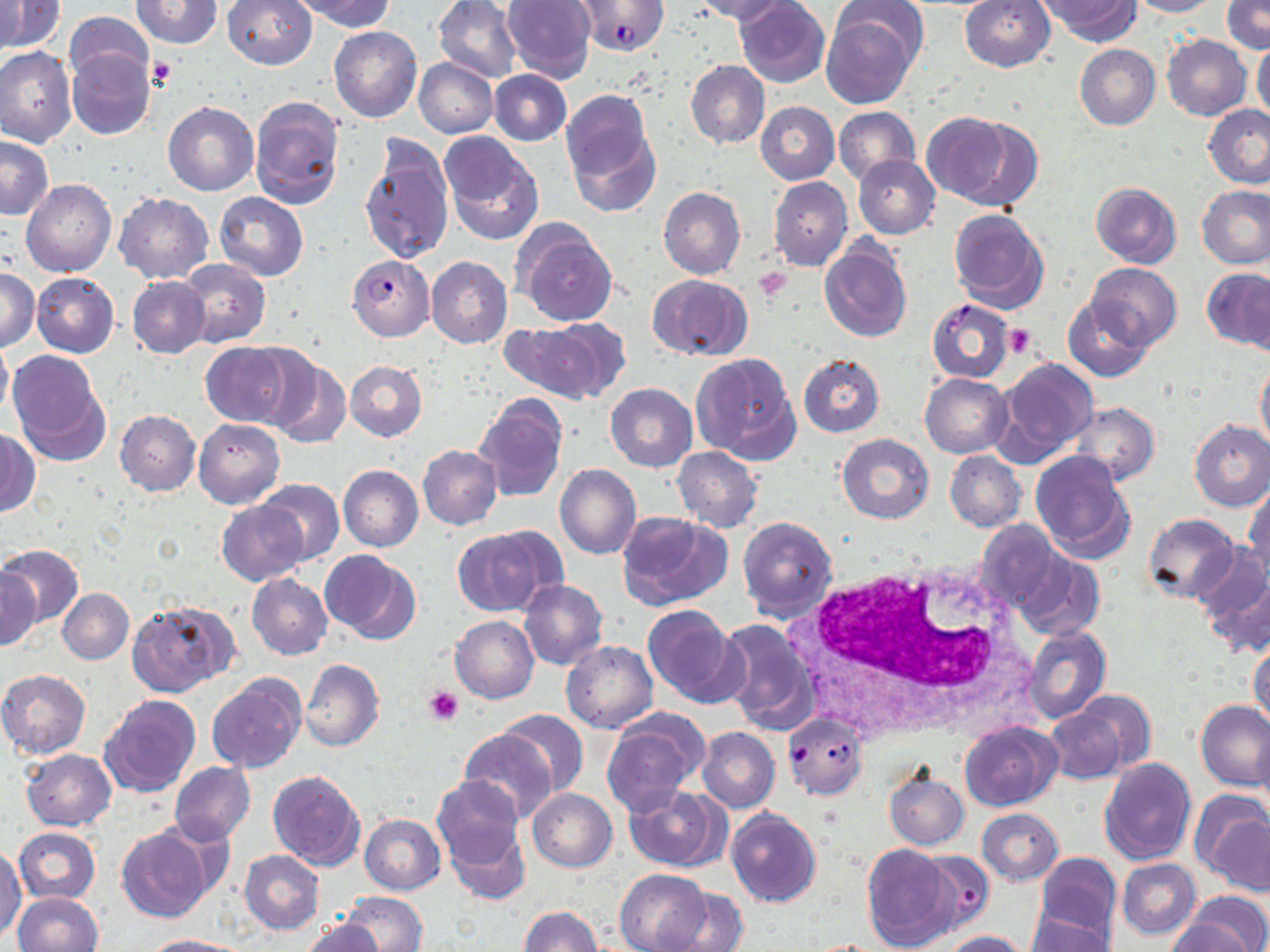
Approximate bounding boxes as named x1/y1/x2/y2 corners in pixels. White blood cell locations: (x1=792, y1=554, x2=1030, y2=734). Platelet locations: (x1=147, y1=57, x2=177, y2=90), (x1=753, y1=265, x2=794, y2=302), (x1=1003, y1=324, x2=1036, y2=359), (x1=422, y1=686, x2=464, y2=726). Uninfected red blood cell locations: (x1=132, y1=0, x2=222, y2=47), (x1=222, y1=0, x2=318, y2=70), (x1=433, y1=0, x2=522, y2=83), (x1=503, y1=0, x2=596, y2=81), (x1=734, y1=0, x2=829, y2=87), (x1=959, y1=0, x2=1055, y2=72), (x1=1129, y1=0, x2=1221, y2=18), (x1=1, y1=1, x2=20, y2=59), (x1=299, y1=1, x2=397, y2=31), (x1=692, y1=1, x2=788, y2=23), (x1=1038, y1=1, x2=1138, y2=44), (x1=1221, y1=1, x2=1269, y2=53), (x1=1, y1=2, x2=64, y2=53), (x1=821, y1=6, x2=919, y2=109), (x1=65, y1=10, x2=153, y2=87), (x1=328, y1=25, x2=423, y2=123), (x1=1162, y1=34, x2=1251, y2=120), (x1=1252, y1=38, x2=1270, y2=123), (x1=1074, y1=43, x2=1161, y2=130), (x1=0, y1=47, x2=76, y2=149), (x1=68, y1=51, x2=154, y2=139), (x1=414, y1=59, x2=497, y2=138), (x1=685, y1=60, x2=769, y2=149), (x1=488, y1=69, x2=571, y2=146), (x1=562, y1=93, x2=658, y2=215), (x1=249, y1=95, x2=344, y2=209), (x1=163, y1=101, x2=258, y2=197), (x1=756, y1=102, x2=839, y2=185), (x1=1202, y1=103, x2=1270, y2=189), (x1=833, y1=106, x2=919, y2=184), (x1=920, y1=112, x2=1030, y2=207), (x1=441, y1=136, x2=543, y2=244), (x1=0, y1=137, x2=53, y2=219), (x1=359, y1=138, x2=455, y2=264), (x1=852, y1=153, x2=940, y2=240), (x1=768, y1=177, x2=853, y2=271), (x1=21, y1=178, x2=116, y2=277), (x1=1091, y1=182, x2=1182, y2=268), (x1=1196, y1=184, x2=1270, y2=269), (x1=658, y1=188, x2=745, y2=279), (x1=114, y1=192, x2=212, y2=282), (x1=214, y1=192, x2=307, y2=280), (x1=947, y1=209, x2=1049, y2=313), (x1=514, y1=225, x2=617, y2=326), (x1=819, y1=239, x2=912, y2=343), (x1=426, y1=256, x2=513, y2=349), (x1=178, y1=259, x2=270, y2=347), (x1=1088, y1=263, x2=1181, y2=350), (x1=1202, y1=267, x2=1270, y2=350), (x1=1, y1=268, x2=40, y2=353), (x1=31, y1=272, x2=119, y2=357), (x1=648, y1=275, x2=751, y2=360), (x1=127, y1=276, x2=210, y2=357), (x1=1063, y1=298, x2=1152, y2=381), (x1=504, y1=318, x2=625, y2=403), (x1=0, y1=340, x2=12, y2=421), (x1=200, y1=342, x2=297, y2=427), (x1=6, y1=352, x2=107, y2=465), (x1=691, y1=352, x2=800, y2=465), (x1=798, y1=353, x2=884, y2=437), (x1=266, y1=357, x2=350, y2=449), (x1=993, y1=357, x2=1098, y2=464), (x1=344, y1=361, x2=427, y2=441), (x1=1256, y1=362, x2=1270, y2=457), (x1=920, y1=373, x2=1012, y2=458), (x1=606, y1=383, x2=697, y2=472), (x1=474, y1=394, x2=568, y2=502), (x1=1071, y1=403, x2=1159, y2=484), (x1=114, y1=411, x2=200, y2=495), (x1=194, y1=418, x2=284, y2=509), (x1=1189, y1=420, x2=1270, y2=511), (x1=0, y1=427, x2=39, y2=516), (x1=836, y1=434, x2=934, y2=524), (x1=417, y1=445, x2=502, y2=530), (x1=672, y1=447, x2=763, y2=532), (x1=1031, y1=449, x2=1135, y2=562), (x1=945, y1=451, x2=1025, y2=532), (x1=555, y1=465, x2=641, y2=560), (x1=338, y1=466, x2=424, y2=550), (x1=257, y1=479, x2=344, y2=564), (x1=1245, y1=483, x2=1270, y2=576), (x1=217, y1=501, x2=310, y2=585), (x1=616, y1=510, x2=732, y2=612), (x1=737, y1=514, x2=838, y2=621), (x1=1142, y1=514, x2=1238, y2=603), (x1=975, y1=520, x2=1065, y2=616), (x1=453, y1=527, x2=556, y2=617), (x1=0, y1=544, x2=83, y2=625), (x1=1191, y1=545, x2=1270, y2=636), (x1=321, y1=550, x2=422, y2=645), (x1=1015, y1=552, x2=1104, y2=642), (x1=1, y1=567, x2=41, y2=650), (x1=247, y1=573, x2=333, y2=659), (x1=518, y1=580, x2=607, y2=670), (x1=58, y1=588, x2=133, y2=664), (x1=129, y1=599, x2=240, y2=696), (x1=642, y1=604, x2=744, y2=709), (x1=450, y1=616, x2=540, y2=704), (x1=714, y1=618, x2=820, y2=734), (x1=1023, y1=626, x2=1111, y2=724), (x1=1249, y1=638, x2=1270, y2=730), (x1=562, y1=642, x2=657, y2=732), (x1=300, y1=659, x2=384, y2=751), (x1=0, y1=669, x2=90, y2=758), (x1=207, y1=673, x2=306, y2=774), (x1=1069, y1=691, x2=1157, y2=774), (x1=101, y1=694, x2=201, y2=795), (x1=1196, y1=700, x2=1270, y2=792), (x1=1043, y1=706, x2=1128, y2=784), (x1=499, y1=709, x2=589, y2=798), (x1=602, y1=715, x2=706, y2=815), (x1=960, y1=723, x2=1060, y2=810), (x1=696, y1=727, x2=780, y2=812), (x1=459, y1=729, x2=554, y2=821), (x1=1254, y1=730, x2=1270, y2=818), (x1=20, y1=748, x2=116, y2=831), (x1=1100, y1=758, x2=1195, y2=865), (x1=170, y1=761, x2=254, y2=844), (x1=157, y1=767, x2=245, y2=909), (x1=883, y1=769, x2=968, y2=849), (x1=267, y1=770, x2=366, y2=871), (x1=432, y1=775, x2=524, y2=867), (x1=623, y1=785, x2=726, y2=871), (x1=527, y1=787, x2=617, y2=871), (x1=1192, y1=791, x2=1270, y2=891), (x1=978, y1=808, x2=1063, y2=885), (x1=725, y1=809, x2=822, y2=908), (x1=359, y1=814, x2=445, y2=894), (x1=445, y1=821, x2=529, y2=905), (x1=14, y1=827, x2=101, y2=904), (x1=116, y1=827, x2=212, y2=923), (x1=861, y1=844, x2=960, y2=951), (x1=0, y1=849, x2=23, y2=939), (x1=239, y1=850, x2=324, y2=933), (x1=1035, y1=853, x2=1121, y2=941), (x1=1117, y1=858, x2=1201, y2=940), (x1=614, y1=869, x2=711, y2=952), (x1=661, y1=887, x2=750, y2=952), (x1=339, y1=891, x2=428, y2=952), (x1=13, y1=892, x2=104, y2=952), (x1=1179, y1=894, x2=1270, y2=952), (x1=520, y1=906, x2=602, y2=952), (x1=1025, y1=909, x2=1115, y2=952), (x1=1164, y1=918, x2=1255, y2=952), (x1=301, y1=919, x2=384, y2=952), (x1=941, y1=930, x2=1030, y2=952), (x1=143, y1=935, x2=250, y2=952). Plasmodium falciparum-infected red blood cell locations: (x1=576, y1=1, x2=668, y2=56), (x1=347, y1=254, x2=435, y2=341), (x1=927, y1=299, x2=1015, y2=384), (x1=782, y1=712, x2=867, y2=800), (x1=917, y1=851, x2=996, y2=931). Slide-level diagnosis: Plasmodium falciparum. Optical microscopy. Single field of view. Image is 1270×952 pixels. Thin blood film. 1000x magnification. May-Grünwald-Giemsa stain.